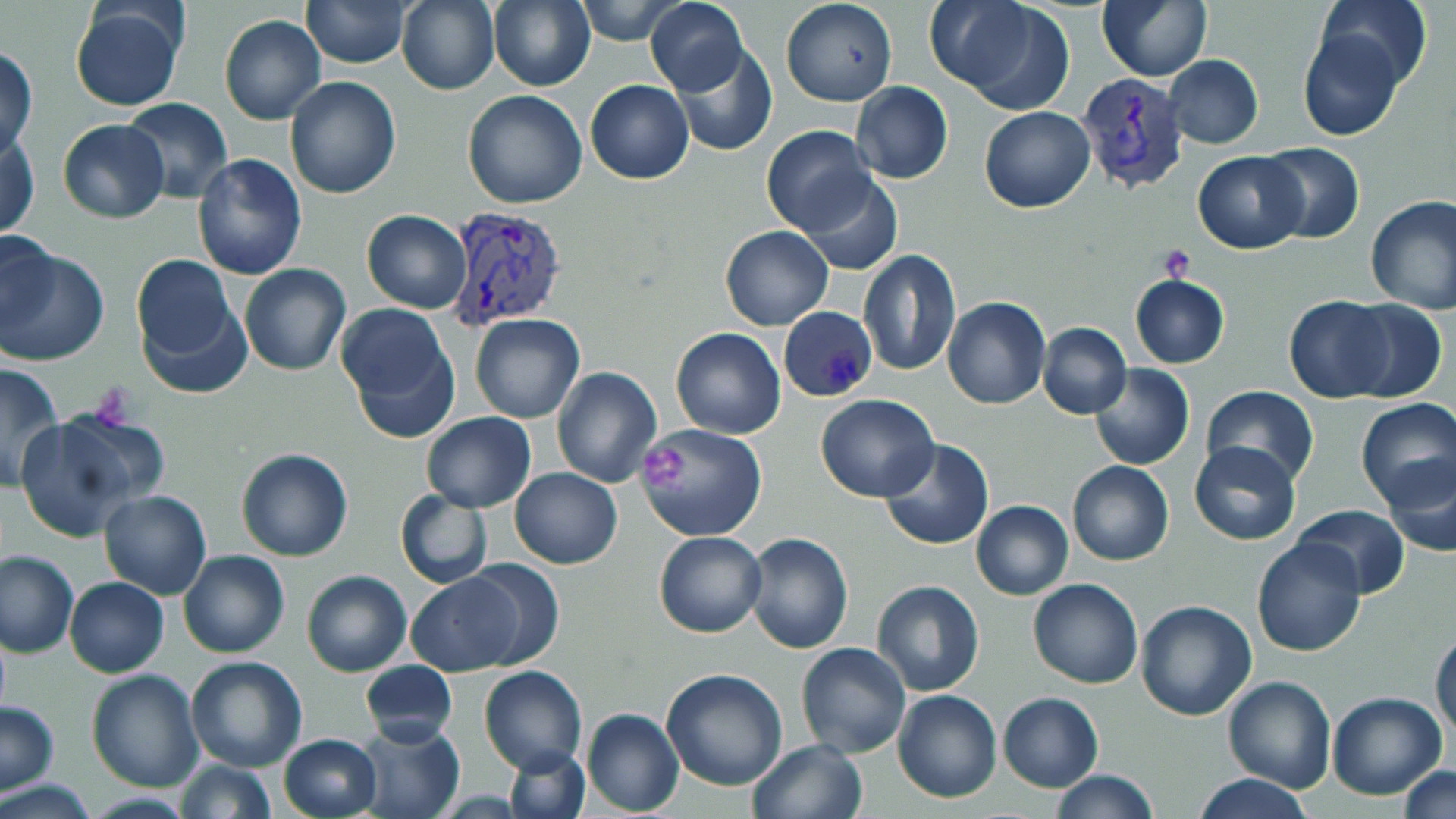

slide-level diagnosis = Plasmodium vivax
uninfected red blood cell locations = approximate bounding boxes as (x1, y1, x2, y2) in pixels: (395, 0, 501, 96), (487, 0, 596, 93), (574, 0, 684, 46), (644, 0, 748, 98), (781, 0, 898, 106), (934, 0, 1077, 113), (1098, 0, 1212, 81), (1315, 0, 1433, 91), (303, 1, 411, 68), (68, 3, 191, 114), (219, 14, 327, 124), (1297, 27, 1404, 142), (671, 45, 778, 157), (1, 46, 37, 161), (1163, 55, 1264, 149), (284, 75, 402, 200), (585, 80, 693, 185), (849, 82, 953, 185), (462, 90, 587, 209), (118, 96, 233, 203), (979, 106, 1095, 213), (57, 118, 170, 224), (761, 125, 875, 235), (1, 131, 40, 241), (1258, 142, 1366, 244), (1192, 151, 1308, 253), (192, 153, 307, 282), (796, 169, 904, 277), (1364, 194, 1456, 314), (361, 211, 472, 313), (720, 225, 833, 330), (0, 227, 63, 337), (0, 241, 107, 366), (858, 250, 962, 376), (131, 253, 244, 380), (239, 264, 350, 376), (1130, 275, 1230, 370), (1284, 295, 1392, 404), (942, 296, 1050, 409), (1343, 298, 1447, 404), (337, 303, 460, 443), (470, 313, 585, 424), (1037, 321, 1131, 419), (670, 329, 785, 438), (1, 361, 65, 489), (1089, 363, 1194, 470), (552, 366, 663, 489), (1090, 373, 1310, 473), (1201, 384, 1318, 488), (816, 395, 940, 503), (1354, 398, 1456, 511), (13, 412, 155, 543), (421, 412, 535, 512), (635, 420, 767, 541), (881, 438, 995, 551), (1190, 440, 1300, 546), (237, 448, 352, 562), (1381, 459, 1456, 558), (1067, 461, 1175, 567), (509, 468, 622, 569), (99, 489, 212, 599), (394, 490, 492, 589), (971, 500, 1074, 600), (1291, 504, 1412, 599), (654, 530, 766, 639), (742, 532, 854, 653), (1251, 536, 1366, 657), (179, 549, 290, 659), (0, 550, 78, 657), (462, 559, 564, 671), (301, 569, 412, 678), (407, 572, 521, 677), (63, 577, 168, 678), (1028, 579, 1144, 688), (870, 580, 986, 697), (1135, 598, 1257, 721), (1431, 627, 1456, 740), (795, 641, 911, 758), (185, 655, 307, 771), (359, 658, 458, 744), (479, 665, 587, 776), (85, 668, 204, 793), (659, 669, 788, 792), (1223, 674, 1337, 792), (894, 690, 1003, 803), (997, 691, 1104, 793), (1326, 691, 1448, 801), (1, 699, 59, 793), (581, 708, 683, 816), (356, 720, 465, 818), (278, 734, 381, 819), (746, 738, 869, 819), (503, 744, 591, 819), (171, 759, 277, 817), (1397, 765, 1456, 819), (1050, 771, 1160, 818), (1192, 773, 1315, 818), (0, 778, 102, 817)
preparation = thin blood smear
field of view = single
image size = 1456×819 pixels
modality = optical microscopy
stain = May-Grünwald-Giemsa
Plasmodium vivax-infected red blood cell locations = approximate bounding boxes as (x1, y1, x2, y2) in pixels: (1078, 72, 1191, 194), (443, 208, 568, 332), (779, 305, 879, 402)
platelet locations = approximate bounding boxes as (x1, y1, x2, y2) in pixels: (1161, 245, 1195, 281), (90, 383, 138, 425), (640, 440, 687, 491)
magnification = 1000x